Locate and identify every blood parasite.
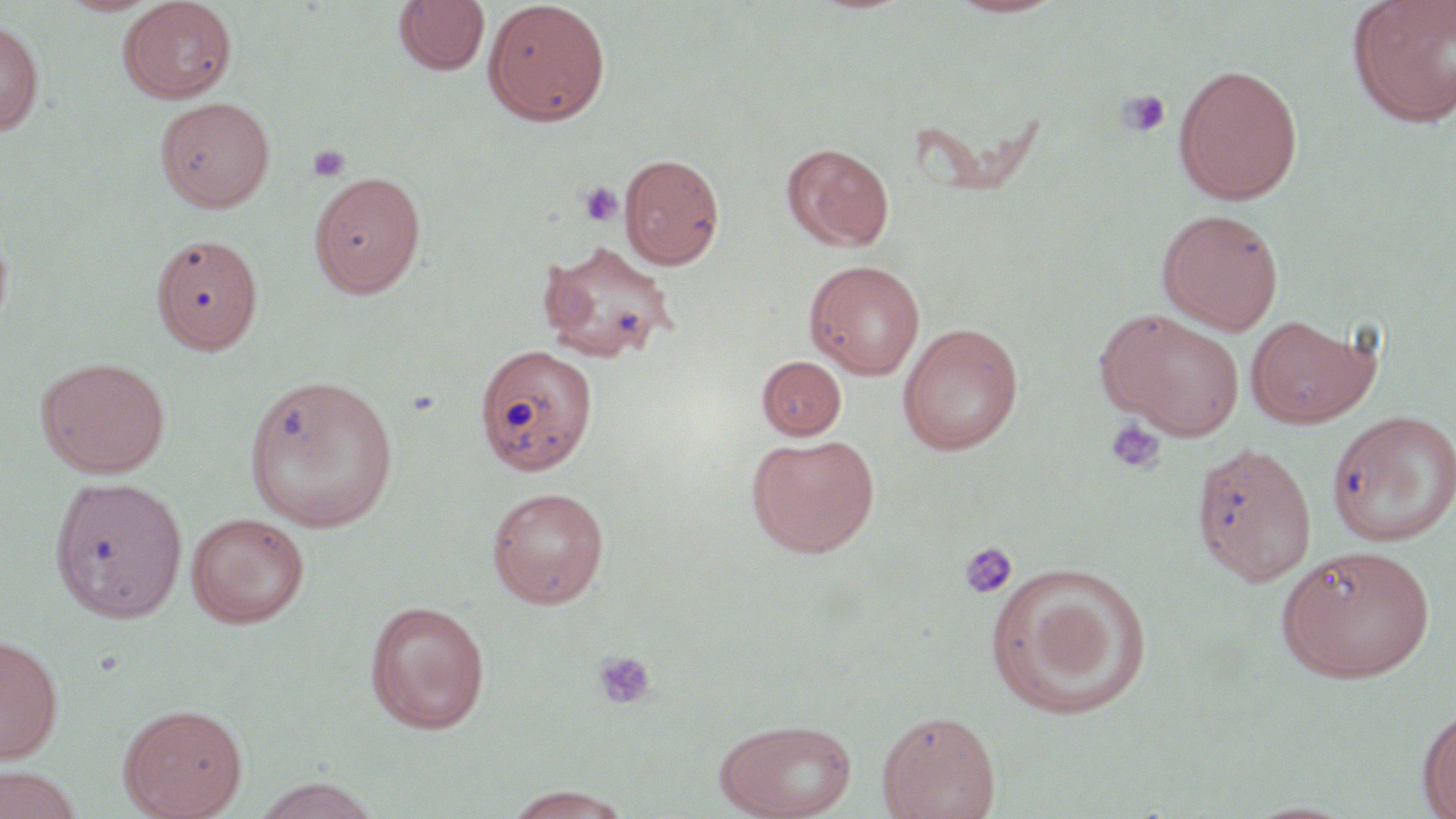

No blood parasites seen.

Summary:
  - Coordinate format: approximate bounding boxes as named x1/y1/x2/y2 corners in pixels
  - Uninfected red blood cell locations: (x1=947, y1=0, x2=1065, y2=19), (x1=58, y1=1, x2=159, y2=17), (x1=120, y1=1, x2=237, y2=102), (x1=393, y1=1, x2=490, y2=76), (x1=482, y1=1, x2=610, y2=126), (x1=1347, y1=1, x2=1456, y2=128), (x1=1392, y1=1, x2=1456, y2=45), (x1=0, y1=18, x2=45, y2=136), (x1=1173, y1=62, x2=1303, y2=205), (x1=156, y1=96, x2=275, y2=212), (x1=781, y1=142, x2=894, y2=251), (x1=619, y1=153, x2=725, y2=269), (x1=309, y1=169, x2=426, y2=297), (x1=1157, y1=208, x2=1283, y2=334), (x1=0, y1=219, x2=14, y2=339), (x1=537, y1=240, x2=679, y2=364), (x1=805, y1=259, x2=925, y2=380), (x1=1099, y1=309, x2=1246, y2=439), (x1=1244, y1=314, x2=1378, y2=428), (x1=898, y1=322, x2=1023, y2=455), (x1=474, y1=343, x2=597, y2=476), (x1=36, y1=356, x2=171, y2=478), (x1=757, y1=356, x2=847, y2=440), (x1=243, y1=373, x2=400, y2=532), (x1=1326, y1=409, x2=1456, y2=547), (x1=747, y1=434, x2=880, y2=558), (x1=1191, y1=443, x2=1317, y2=587), (x1=48, y1=476, x2=189, y2=623), (x1=486, y1=486, x2=610, y2=608), (x1=185, y1=511, x2=310, y2=629), (x1=1277, y1=544, x2=1435, y2=684), (x1=988, y1=564, x2=1152, y2=721), (x1=364, y1=599, x2=491, y2=733), (x1=0, y1=633, x2=64, y2=764), (x1=118, y1=702, x2=248, y2=819), (x1=1417, y1=705, x2=1456, y2=819), (x1=876, y1=709, x2=1001, y2=819), (x1=715, y1=717, x2=858, y2=819), (x1=0, y1=765, x2=85, y2=819), (x1=252, y1=777, x2=384, y2=819), (x1=502, y1=785, x2=637, y2=819), (x1=1243, y1=799, x2=1360, y2=818)
  - Platelet locations: (x1=1116, y1=89, x2=1171, y2=137), (x1=308, y1=143, x2=352, y2=183), (x1=579, y1=182, x2=623, y2=227), (x1=1105, y1=419, x2=1165, y2=475), (x1=959, y1=541, x2=1018, y2=599), (x1=593, y1=651, x2=657, y2=710)
  - Slide-level diagnosis: negative for blood parasites
  - Modality: optical microscopy
  - Magnification: 1000x
  - Stain: May-Grünwald-Giemsa
  - Field of view: single
  - Preparation: thin blood film
  - Image size: 1456×819 pixels